Comment on the morphology of the erythrocytes.
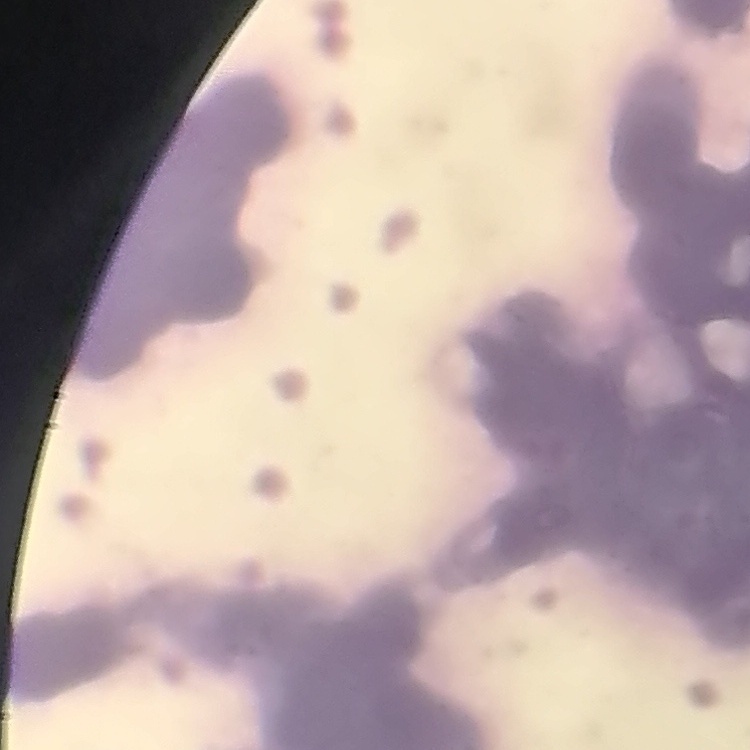
Rouleaux formation.

stain = Field's or Giemsa
image type = square crop of a larger photomicrograph
preparation = thin peripheral smear